State which parasite is depicted.
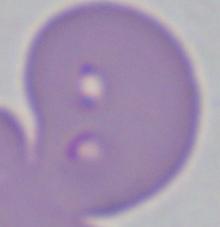
This is Babesia.

magnification = 1000x
modality = photomicrograph